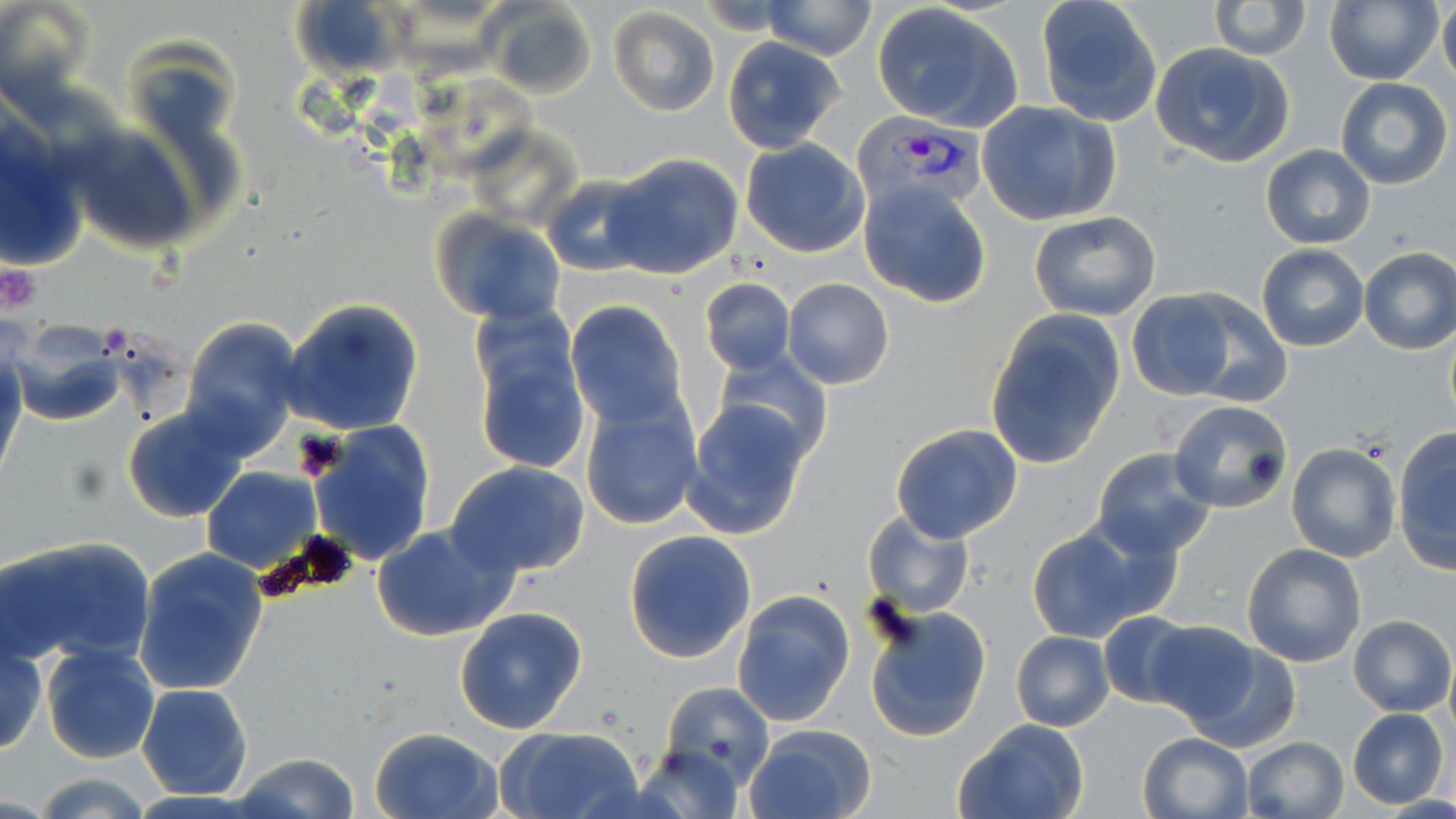 Approximate bounding boxes as [x1, y1, x2, y2] in pixels. Plasmodium vivax-infected red blood cell locations: [853, 115, 988, 215]. Uninfected red blood cell locations: [0, 0, 96, 109], [290, 0, 401, 78], [1208, 0, 1311, 59], [1439, 0, 1456, 93], [760, 1, 879, 59], [1034, 1, 1160, 127], [1324, 1, 1443, 86], [871, 3, 1025, 132], [487, 4, 597, 98], [607, 6, 720, 116], [723, 37, 846, 154], [1150, 43, 1297, 170], [1335, 78, 1452, 189], [978, 102, 1122, 227], [0, 121, 87, 273], [69, 128, 200, 254], [740, 139, 871, 258], [1260, 144, 1376, 250], [606, 154, 742, 278], [543, 175, 654, 274], [859, 179, 993, 310], [433, 209, 566, 326], [1029, 209, 1162, 322], [1257, 244, 1368, 351], [1358, 246, 1456, 355], [781, 277, 894, 390], [699, 278, 795, 375], [1123, 291, 1241, 402], [1172, 291, 1292, 406], [283, 298, 424, 436], [566, 301, 687, 432], [469, 307, 592, 481], [984, 312, 1125, 469], [179, 316, 303, 458], [7, 318, 129, 426], [713, 349, 835, 463], [0, 350, 25, 470], [579, 397, 701, 529], [682, 400, 811, 540], [1167, 400, 1294, 517], [121, 406, 247, 524], [308, 421, 437, 565], [889, 423, 1023, 544], [1393, 430, 1456, 574], [1286, 444, 1399, 564], [1092, 448, 1217, 560], [444, 460, 593, 580], [201, 467, 322, 574], [861, 508, 976, 620], [371, 523, 519, 642], [1026, 527, 1150, 643], [623, 529, 757, 665], [3, 534, 156, 668], [1241, 543, 1368, 668], [133, 547, 270, 697], [731, 589, 856, 728], [864, 604, 993, 740], [454, 606, 588, 735], [1095, 611, 1203, 709], [1349, 614, 1454, 716], [1141, 620, 1262, 725], [1, 631, 49, 756], [1011, 631, 1114, 730], [41, 639, 161, 765], [1177, 639, 1301, 754], [136, 683, 253, 801], [658, 683, 776, 790], [1348, 708, 1449, 808], [953, 719, 1090, 819], [744, 725, 877, 819], [369, 726, 502, 819], [494, 726, 645, 819], [1137, 733, 1253, 819], [1240, 736, 1349, 818], [632, 744, 745, 818], [232, 753, 361, 819], [29, 772, 159, 819]. Platelet locations: [0, 260, 43, 315], [101, 326, 125, 352]. Slide-level diagnosis: Plasmodium vivax. Light microscopy. Single field of view. Captured at 1000x magnification. May-Grünwald-Giemsa stain. Image is 1456×819 pixels. Thin blood film.